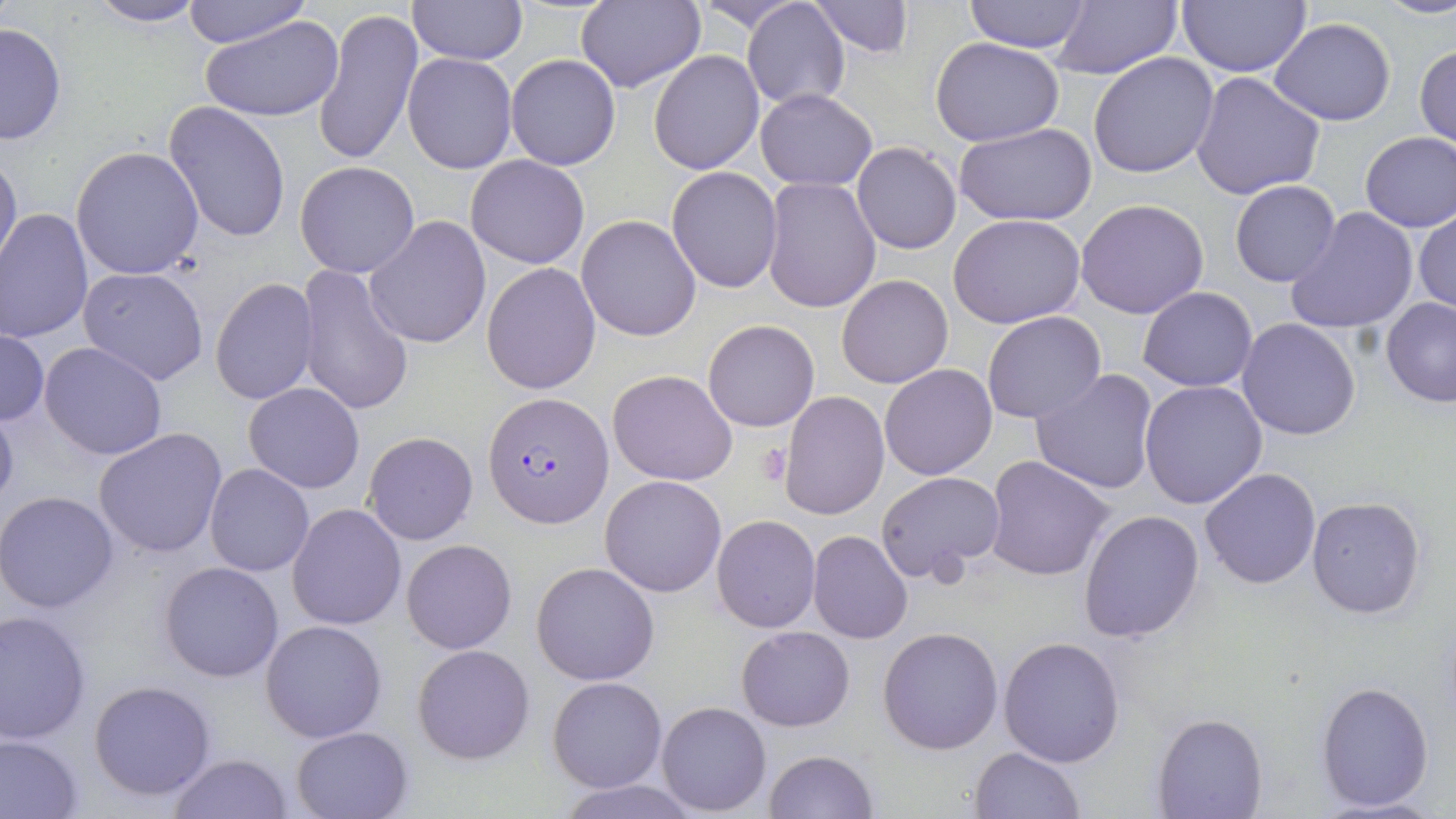

Summary:
  - Coordinate format: approximate bounding boxes as (x1,y1)-(x2,y2) corner pairs in pixels
  - Uninfected red blood cell locations: (183,0)-(311,47), (408,0)-(527,66), (574,0)-(705,92), (694,0)-(804,32), (809,0)-(913,57), (962,0)-(1093,54), (1176,0)-(1311,77), (1382,0)-(1456,20), (85,1)-(209,28), (741,1)-(850,110), (1052,3)-(1181,78), (312,7)-(420,168), (200,15)-(344,123), (1268,17)-(1396,126), (0,21)-(68,146), (932,38)-(1063,147), (1415,43)-(1456,153), (648,49)-(764,175), (1088,51)-(1220,179), (402,52)-(518,174), (505,55)-(620,171), (1190,71)-(1326,201), (754,88)-(877,190), (164,102)-(291,242), (955,124)-(1100,227), (1360,130)-(1456,232), (851,141)-(962,254), (71,147)-(204,281), (0,148)-(22,272), (466,155)-(590,270), (294,161)-(420,279), (665,166)-(784,294), (761,178)-(882,313), (1229,179)-(1341,287), (1075,199)-(1208,319), (1286,206)-(1421,334), (1,209)-(95,343), (1413,210)-(1455,317), (949,213)-(1088,329), (575,214)-(703,342), (364,216)-(492,348), (481,261)-(601,395), (296,264)-(415,416), (78,266)-(210,386), (837,275)-(954,389), (209,277)-(320,406), (1138,287)-(1258,392), (1381,297)-(1456,406), (982,311)-(1106,423), (1237,318)-(1363,441), (703,319)-(820,432), (0,329)-(49,427), (38,341)-(168,461), (879,364)-(999,480), (609,369)-(738,487), (1030,369)-(1161,496), (1138,379)-(1267,510), (243,382)-(364,493), (777,390)-(889,521), (0,405)-(19,517), (93,426)-(229,559), (363,432)-(478,545), (985,456)-(1114,581), (204,464)-(315,579), (1199,467)-(1323,589), (874,470)-(1006,585), (599,475)-(726,596), (0,492)-(119,614), (1306,496)-(1427,618), (285,502)-(409,631), (1079,511)-(1205,643), (711,514)-(821,633), (807,530)-(913,644), (401,539)-(517,654), (158,561)-(285,683), (531,562)-(660,685), (0,609)-(92,744), (260,618)-(387,742), (878,626)-(1004,755), (736,627)-(856,730), (997,636)-(1126,767), (412,643)-(536,765), (548,676)-(668,792), (88,679)-(218,802), (1315,680)-(1435,812), (656,700)-(771,816), (1152,712)-(1267,818), (291,726)-(412,818), (0,733)-(86,817), (969,746)-(1086,818), (764,750)-(878,819), (168,754)-(295,818), (561,780)-(698,818)
  - Plasmodium falciparum-infected red blood cell locations: (482,390)-(614,528)
  - Platelet locations: (757,443)-(795,486)
  - Slide-level diagnosis: Plasmodium falciparum
  - Field of view: one of a larger specimen
  - Modality: light microscopy
  - Image size: 1456×819 pixels
  - Stain: May-Grünwald-Giemsa
  - Preparation: thin blood film
  - Magnification: 1000x